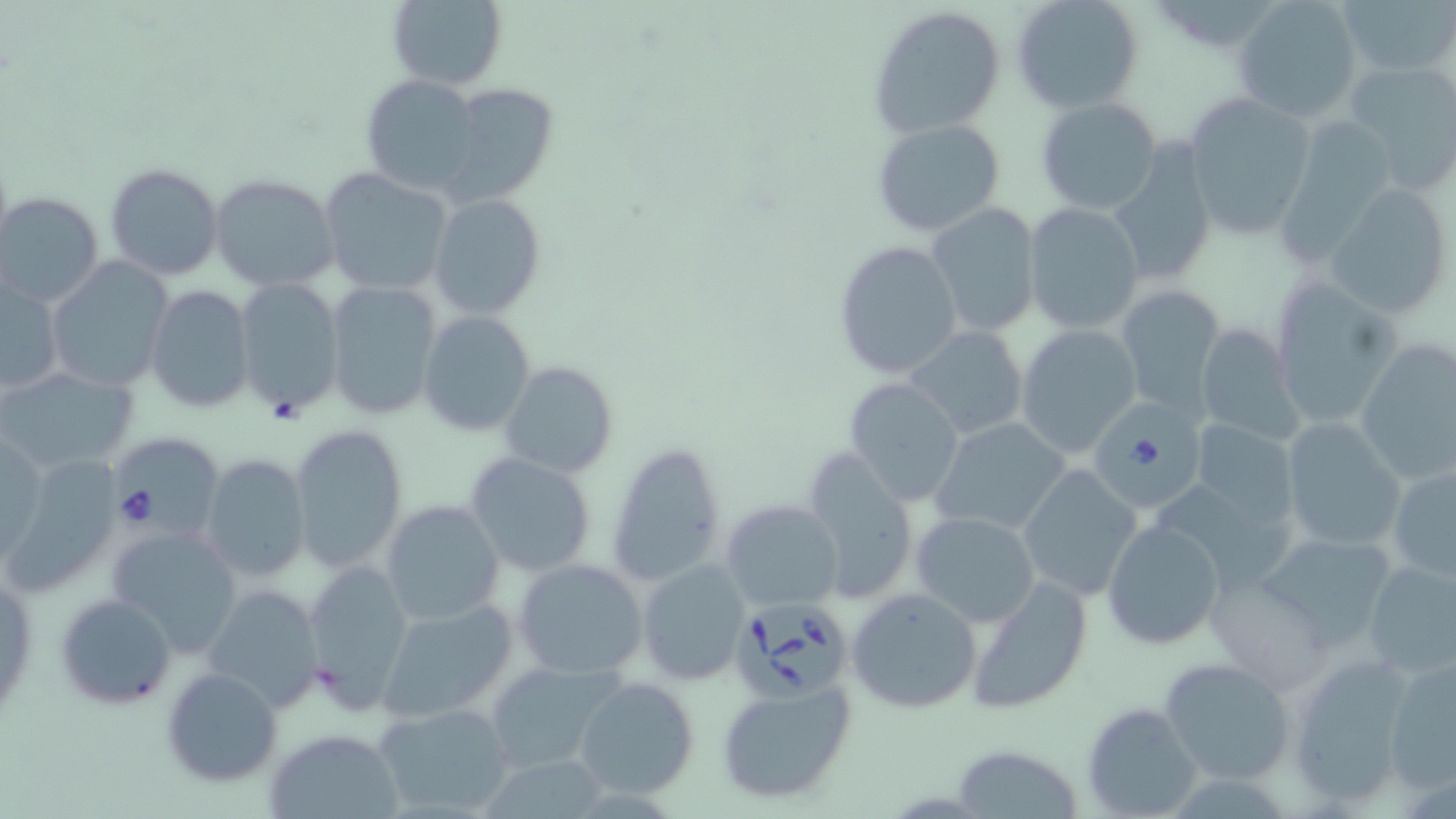 Approximate bounding boxes as (x1, y1, x2, y2) in pixels. Uninfected red blood cell locations: (385, 0, 508, 89), (1011, 0, 1144, 114), (1234, 0, 1361, 122), (1339, 0, 1453, 81), (866, 5, 1006, 137), (1342, 60, 1456, 194), (359, 74, 483, 196), (441, 82, 560, 205), (1181, 92, 1317, 240), (1036, 98, 1165, 216), (872, 119, 1007, 236), (1103, 143, 1217, 286), (105, 163, 226, 281), (320, 167, 454, 297), (210, 175, 340, 290), (1323, 185, 1455, 320), (1, 192, 103, 306), (429, 195, 546, 318), (1024, 202, 1145, 334), (926, 203, 1040, 336), (832, 240, 964, 382), (45, 258, 173, 393), (1, 277, 62, 397), (233, 278, 345, 418), (1267, 279, 1402, 432), (325, 281, 444, 423), (1116, 283, 1227, 418), (146, 287, 256, 413), (418, 310, 537, 436), (1013, 323, 1143, 456), (1195, 323, 1299, 446), (903, 325, 1028, 441), (1354, 337, 1456, 488), (500, 361, 618, 480), (1, 365, 141, 476), (842, 376, 965, 507), (488, 390, 613, 551), (931, 417, 1074, 536), (1188, 418, 1301, 532), (1278, 418, 1406, 553), (286, 421, 410, 572), (1, 428, 48, 561), (607, 441, 728, 586), (800, 450, 920, 604), (198, 452, 313, 584), (464, 453, 596, 576), (1, 455, 122, 596), (1387, 462, 1456, 584), (1016, 465, 1142, 600), (721, 499, 843, 610), (381, 500, 504, 626), (911, 511, 1041, 626), (1102, 519, 1225, 651), (104, 524, 244, 657), (1253, 528, 1402, 651), (1360, 557, 1456, 679), (513, 559, 650, 680), (638, 559, 749, 686), (301, 560, 415, 710), (1, 564, 37, 723), (963, 575, 1094, 714), (202, 584, 325, 712), (846, 588, 982, 715), (55, 593, 177, 710), (377, 597, 520, 726), (1286, 651, 1418, 807), (1384, 653, 1455, 794), (1159, 657, 1295, 785), (483, 660, 628, 773), (161, 666, 281, 787), (573, 674, 700, 801), (716, 682, 856, 804), (371, 701, 519, 818), (1083, 703, 1203, 817), (260, 730, 403, 815), (948, 744, 1085, 819). Babesia divergens-infected red blood cell locations: (1088, 399, 1205, 515), (105, 430, 220, 542), (737, 598, 853, 708). Slide-level diagnosis: Babesia divergens. Image is 1456×819 pixels. 1000x magnification. Single field of view. Thin blood film. May-Grünwald-Giemsa stain. Optical microscopy.